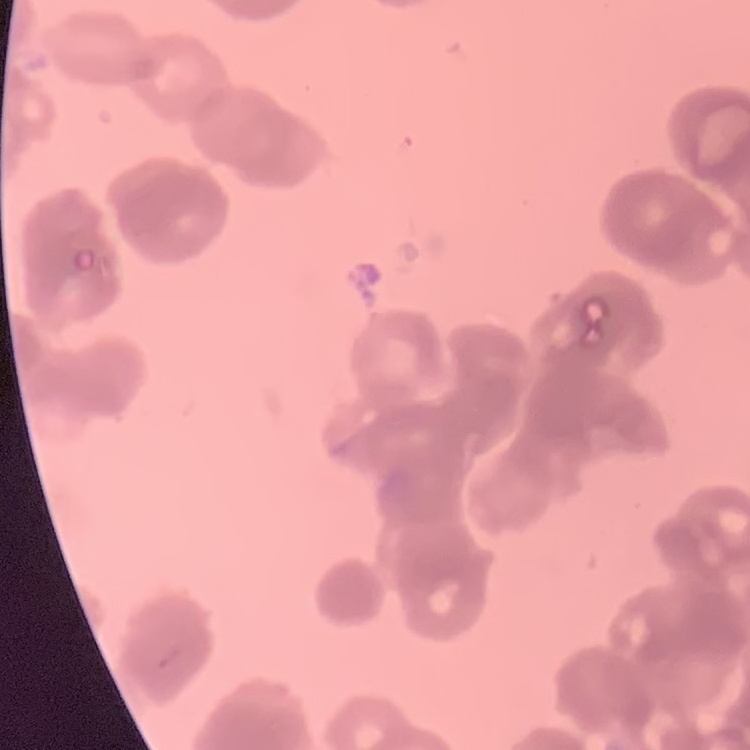 The erythrocytes show rouleaux formation. Square crop of a larger photomicrograph. Thin peripheral smear. Stained with either Field's or Giemsa.